Locate every uninfected red blood cell.
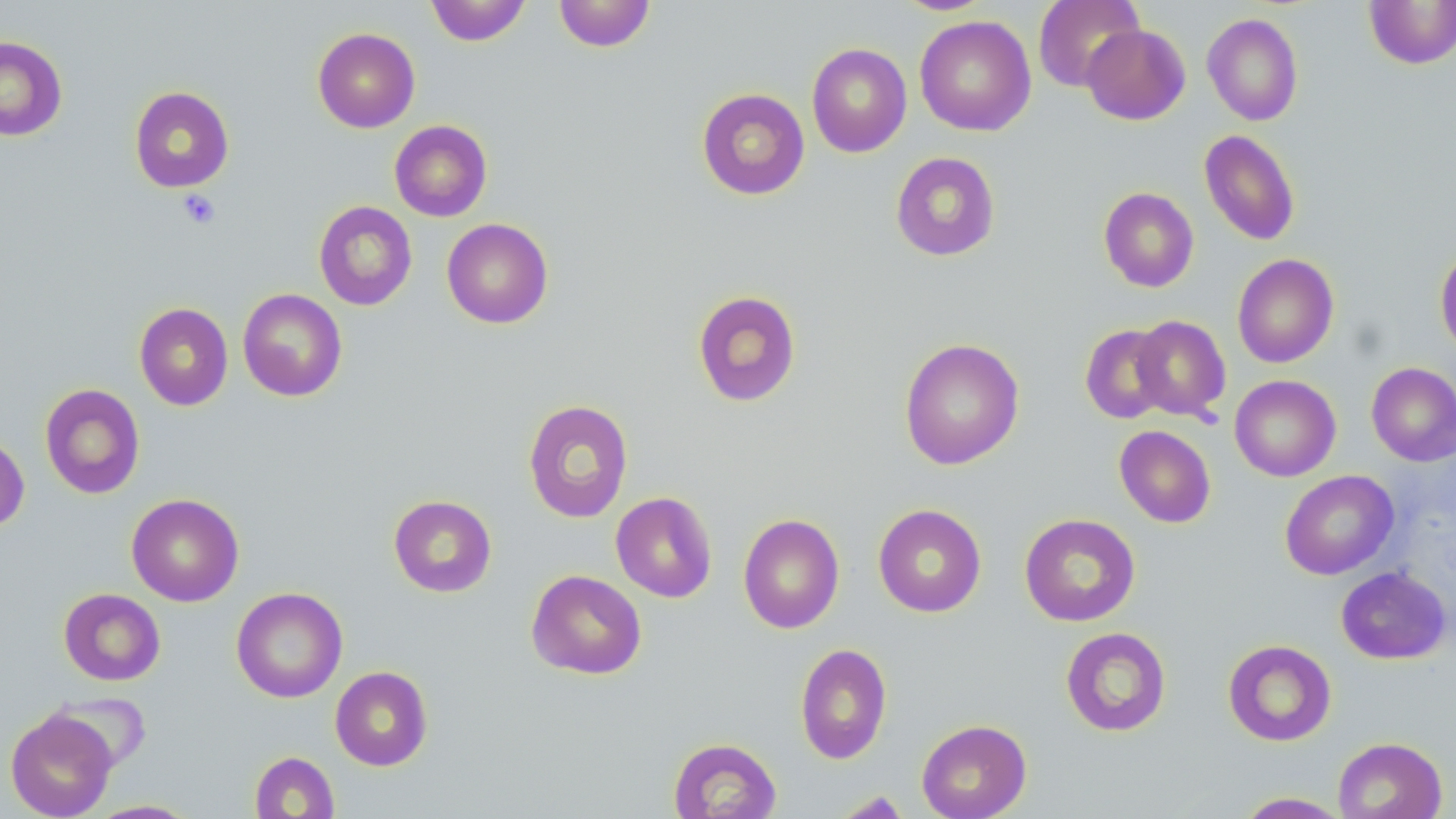

Approximate bounding boxes as [x1, y1, x2, y2] in pixels.
Uninfected red blood cells: [425, 0, 531, 46], [891, 0, 996, 15], [1033, 0, 1144, 92], [1363, 0, 1456, 69], [553, 1, 656, 52], [1202, 12, 1304, 126], [914, 15, 1036, 136], [1081, 24, 1191, 125], [312, 27, 420, 132], [0, 35, 67, 141], [806, 43, 912, 157], [129, 86, 234, 192], [696, 87, 810, 200], [389, 120, 492, 221], [1199, 130, 1300, 246], [890, 151, 1001, 261], [1098, 187, 1199, 292], [314, 201, 417, 311], [441, 218, 553, 329], [1435, 247, 1456, 357], [1232, 253, 1339, 369], [237, 288, 348, 402], [692, 290, 801, 408], [134, 303, 233, 411], [1129, 315, 1231, 422], [1080, 323, 1175, 424], [899, 337, 1024, 470], [1366, 362, 1456, 466], [1229, 375, 1341, 482], [40, 383, 145, 499], [522, 399, 634, 523], [1114, 425, 1216, 527], [0, 432, 29, 533], [1280, 470, 1399, 580], [610, 492, 718, 603], [126, 493, 244, 606], [388, 494, 497, 598], [873, 503, 987, 617], [738, 513, 845, 634], [1018, 513, 1141, 627], [1336, 566, 1452, 665], [526, 569, 647, 680], [231, 587, 347, 703], [59, 588, 166, 686], [1060, 627, 1171, 737], [1223, 639, 1337, 746], [794, 643, 892, 764], [330, 665, 433, 770], [47, 691, 153, 771], [5, 708, 117, 819], [916, 719, 1032, 819], [1332, 736, 1447, 819], [668, 737, 782, 819], [249, 751, 340, 818], [832, 791, 912, 819], [1234, 792, 1351, 818], [86, 799, 202, 818].

slide-level diagnosis = negative for blood parasites
image size = 1456×819 pixels
magnification = 1000x
field of view = one of a larger specimen
stain = May-Grünwald-Giemsa
preparation = thin blood film
platelet locations = approximate bounding boxes as [x1, y1, x2, y2] in pixels: [177, 190, 221, 229]
modality = optical microscopy